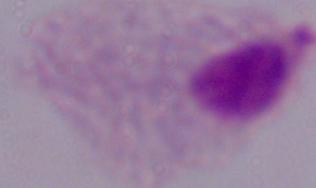
Photomicrograph. Captured at 1000x magnification. A trichomonad is seen.